State which cell type is depicted.
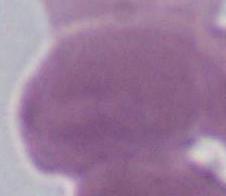

This is an erythrocyte.

magnification: 1000x
modality: photomicrograph